Identify the cell.
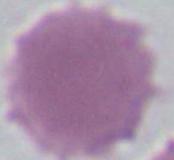

This is an erythrocyte.

Summary:
  - Modality: micrograph
  - Magnification: 1000x